Name the cell type shown.
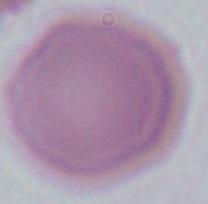
An erythrocyte.

modality: micrograph
magnification: 1000x